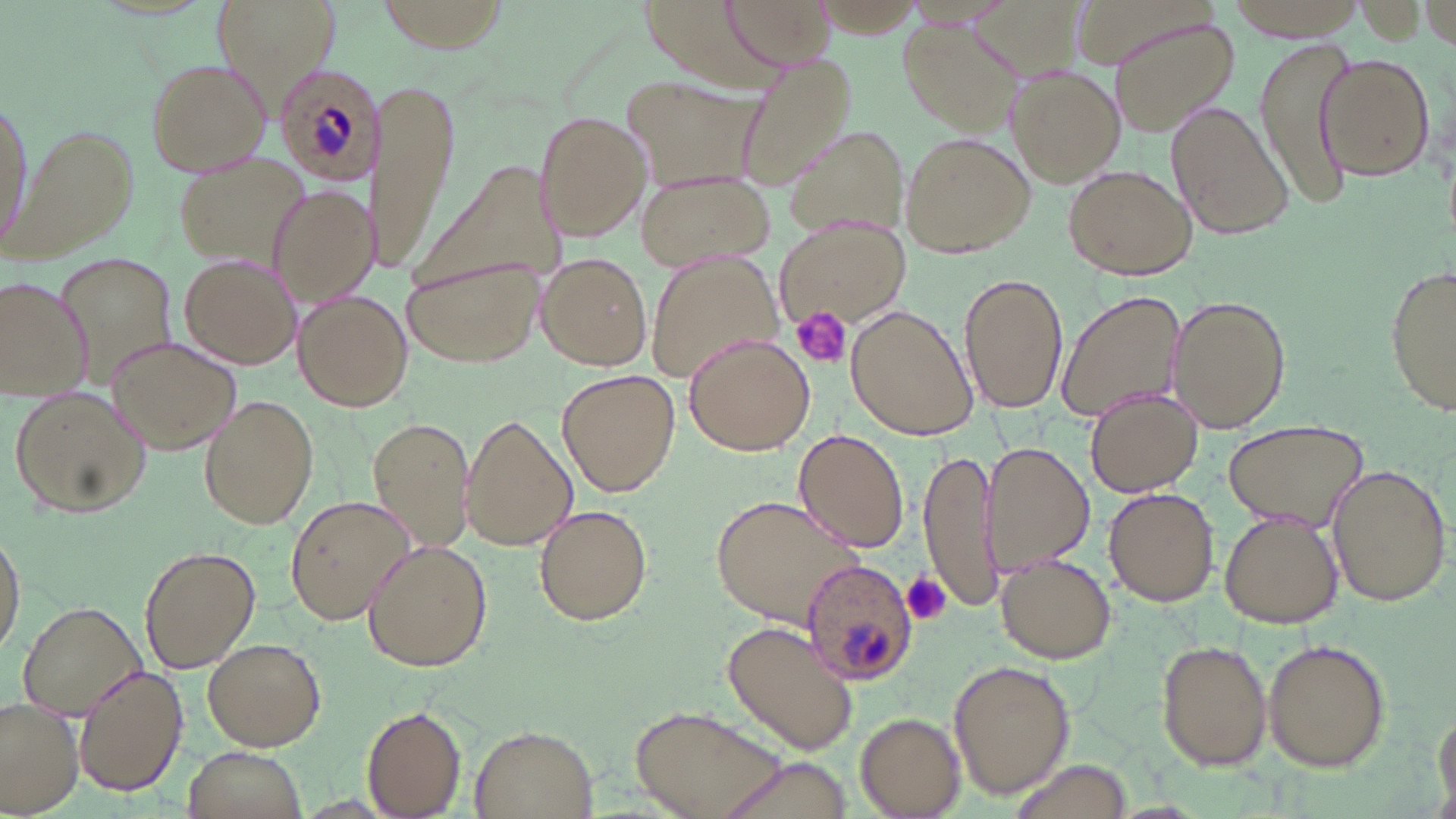
slide-level diagnosis = Plasmodium ovale
uninfected red blood cell locations = approximate bounding boxes as [x1, y1, x2, y2] in pixels: [215, 0, 343, 109], [377, 0, 516, 54], [637, 0, 792, 102], [723, 0, 834, 67], [968, 0, 1095, 91], [1220, 1, 1373, 39], [1109, 14, 1239, 140], [896, 18, 1024, 136], [1252, 34, 1358, 206], [1317, 51, 1436, 180], [732, 53, 858, 192], [146, 59, 271, 176], [1009, 66, 1123, 185], [620, 76, 763, 191], [363, 83, 457, 277], [2, 89, 35, 248], [1167, 101, 1292, 241], [535, 111, 653, 243], [788, 125, 909, 240], [13, 128, 137, 260], [898, 131, 1034, 257], [174, 151, 311, 270], [407, 163, 568, 297], [1063, 164, 1196, 281], [633, 168, 773, 273], [267, 186, 379, 312], [777, 218, 914, 328], [400, 251, 546, 370], [534, 251, 654, 371], [644, 251, 777, 384], [59, 253, 182, 388], [178, 253, 301, 368], [1382, 264, 1456, 421], [959, 271, 1068, 414], [0, 276, 92, 398], [1056, 290, 1187, 424], [292, 292, 410, 412], [1165, 293, 1292, 433], [846, 304, 977, 441], [684, 333, 816, 456], [107, 337, 239, 454], [558, 369, 680, 498], [9, 384, 150, 517], [1084, 388, 1203, 496], [199, 393, 320, 529], [459, 412, 579, 551], [367, 416, 475, 552], [1224, 417, 1371, 529], [794, 428, 909, 553], [986, 440, 1095, 576], [925, 447, 996, 606], [1325, 463, 1453, 608], [1102, 486, 1219, 606], [284, 494, 413, 624], [708, 495, 865, 631], [531, 503, 655, 626], [1219, 509, 1344, 629], [0, 532, 23, 654], [363, 538, 491, 672], [139, 545, 260, 673], [995, 553, 1117, 663], [16, 600, 147, 718], [721, 618, 859, 756], [202, 637, 326, 751], [1262, 638, 1390, 771], [1157, 641, 1273, 770], [949, 659, 1074, 796], [74, 664, 189, 796], [2, 699, 82, 817], [1433, 701, 1455, 814], [361, 705, 467, 817], [632, 705, 789, 818], [854, 713, 966, 819], [468, 725, 599, 819], [183, 744, 307, 818], [713, 756, 853, 818], [1007, 759, 1136, 819]
Plasmodium ovale-infected red blood cell locations = approximate bounding boxes as [x1, y1, x2, y2] in pixels: [275, 63, 383, 188], [798, 557, 917, 684]
image size = 1456×819 pixels
modality = light microscopy
field of view = single
preparation = thin blood smear
stain = May-Grünwald-Giemsa
platelet locations = approximate bounding boxes as [x1, y1, x2, y2] in pixels: [790, 308, 853, 369], [901, 570, 952, 626]
magnification = 1000x